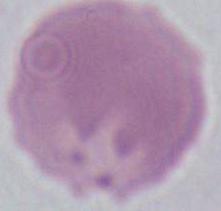

1000x magnification. A red blood cell is shown. Photomicrograph.